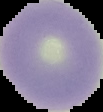
Result: no Plasmodium parasites seen. Segmented cell region on a black background. Image is 103×112 pixels. From a thin blood film.